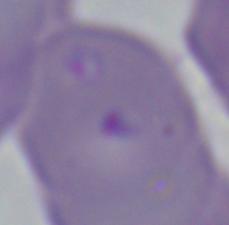
identification = Babesia
magnification = 1000x
modality = photomicrograph